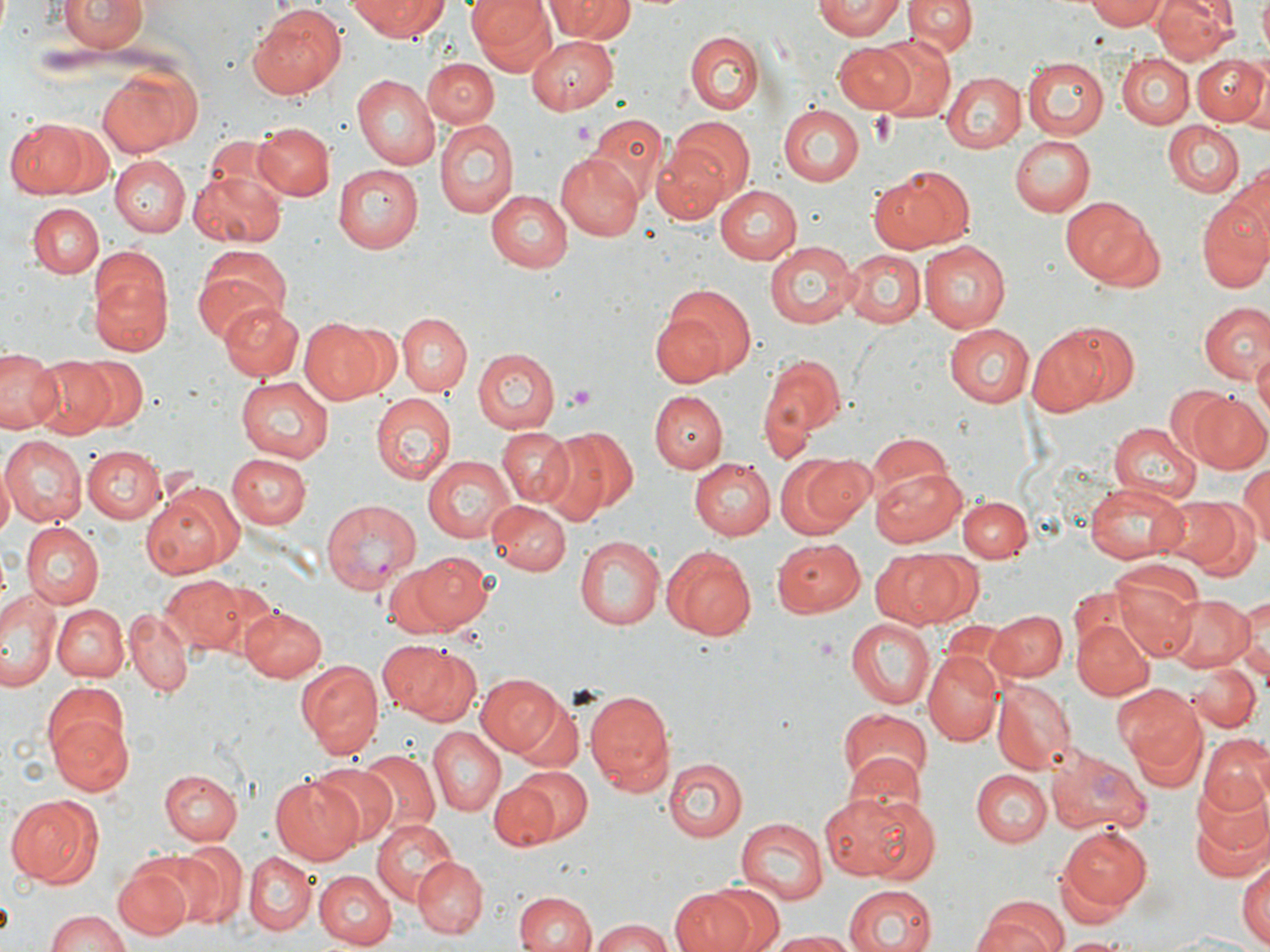

Approximate bounding boxes as (x1,y1)-(x2,y2) corner pairs in pixels. Uninfected red blood cell locations: (61,0)-(147,53), (351,0)-(448,41), (470,0)-(559,78), (811,0)-(907,40), (906,0)-(976,58), (1086,0)-(1168,30), (1153,0)-(1238,64), (1257,0)-(1270,54), (547,2)-(635,42), (245,4)-(349,102), (685,30)-(765,113), (871,33)-(956,121), (527,35)-(618,114), (834,42)-(917,111), (1117,52)-(1193,128), (1192,54)-(1268,128), (1023,56)-(1108,139), (422,58)-(497,128), (98,64)-(197,156), (352,73)-(440,168), (943,73)-(1025,153), (777,104)-(865,186), (588,114)-(667,201), (669,117)-(754,203), (8,118)-(109,199), (435,118)-(517,219), (1162,121)-(1248,198), (252,122)-(333,201), (1010,135)-(1094,216), (651,142)-(733,225), (556,151)-(645,241), (111,157)-(190,236), (332,164)-(423,254), (1222,167)-(1270,269), (868,169)-(970,255), (188,171)-(288,246), (714,184)-(802,265), (485,189)-(574,272), (1197,189)-(1270,293), (1058,197)-(1160,291), (28,203)-(103,280), (920,240)-(1010,333), (766,241)-(857,330), (839,247)-(926,328), (193,248)-(293,339), (90,270)-(172,357), (656,284)-(757,383), (216,301)-(305,380), (1199,303)-(1269,384), (396,312)-(471,396), (298,318)-(388,404), (1059,322)-(1141,407), (943,324)-(1034,406), (1025,326)-(1119,418), (1254,347)-(1270,432), (472,348)-(560,433), (0,349)-(63,433), (29,354)-(115,437), (75,356)-(148,431), (761,358)-(843,446), (236,374)-(333,465), (1162,385)-(1243,466), (650,392)-(727,474), (373,393)-(457,482), (1188,393)-(1270,475), (1109,422)-(1201,504), (542,426)-(637,520), (497,427)-(578,510), (868,434)-(956,509), (1,436)-(85,527), (81,445)-(165,523), (227,453)-(312,529), (772,453)-(869,539), (423,455)-(516,543), (692,456)-(778,540), (1237,461)-(1270,551), (0,464)-(16,540), (869,465)-(968,545), (147,484)-(241,576), (1086,485)-(1184,563), (959,496)-(1031,561), (1156,497)-(1243,572), (488,500)-(571,576), (1189,504)-(1261,586), (18,522)-(102,609), (577,535)-(666,629), (771,539)-(864,617), (661,544)-(757,639), (868,549)-(969,629), (412,552)-(493,629), (382,562)-(460,641), (1109,567)-(1201,663), (158,577)-(246,654), (200,581)-(286,660), (0,589)-(61,690), (1165,594)-(1253,672), (1235,597)-(1269,682), (53,603)-(127,683), (239,605)-(329,681), (984,608)-(1066,681), (125,609)-(192,696), (846,615)-(934,709), (1072,619)-(1153,700), (381,642)-(482,728), (922,649)-(1003,746), (298,661)-(384,757), (1189,662)-(1261,732), (475,674)-(561,756), (993,681)-(1075,773), (585,688)-(675,796), (1118,689)-(1208,782), (510,696)-(584,773), (836,709)-(932,795), (46,710)-(135,798), (428,726)-(506,817), (1201,735)-(1270,816), (360,749)-(439,835), (839,749)-(928,825), (662,759)-(748,842), (309,762)-(400,848), (514,765)-(595,842), (159,768)-(242,846), (971,768)-(1050,845), (271,775)-(367,865), (491,783)-(558,850), (1190,785)-(1269,874), (815,790)-(937,883), (6,796)-(104,889), (736,818)-(827,905), (371,820)-(458,906), (1058,826)-(1152,912), (175,839)-(247,930), (135,848)-(227,932), (244,852)-(316,934), (413,857)-(488,937), (1236,859)-(1269,948), (113,863)-(191,941), (314,871)-(395,948), (709,884)-(784,952), (840,885)-(937,952), (668,887)-(762,952), (514,889)-(597,951), (976,898)-(1069,951), (45,911)-(133,952), (589,918)-(672,952), (765,930)-(856,951), (1158,933)-(1270,952), (1060,936)-(1131,951). Platelet locations: (867,113)-(899,146), (573,120)-(598,145), (565,384)-(598,412). Plasmodium vivax-infected red blood cell locations: (320,497)-(421,593), (1047,745)-(1151,837). Slide-level diagnosis: Plasmodium vivax. Image is 1270×952 pixels. May-Grünwald-Giemsa-stained preparation. Light microscopy. Single field of view. 1000x magnification. Thin blood smear.